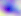 Photomicrograph. Toxoplasma gondii is seen. 400x magnification.